Locate every Plasmodium parasite.
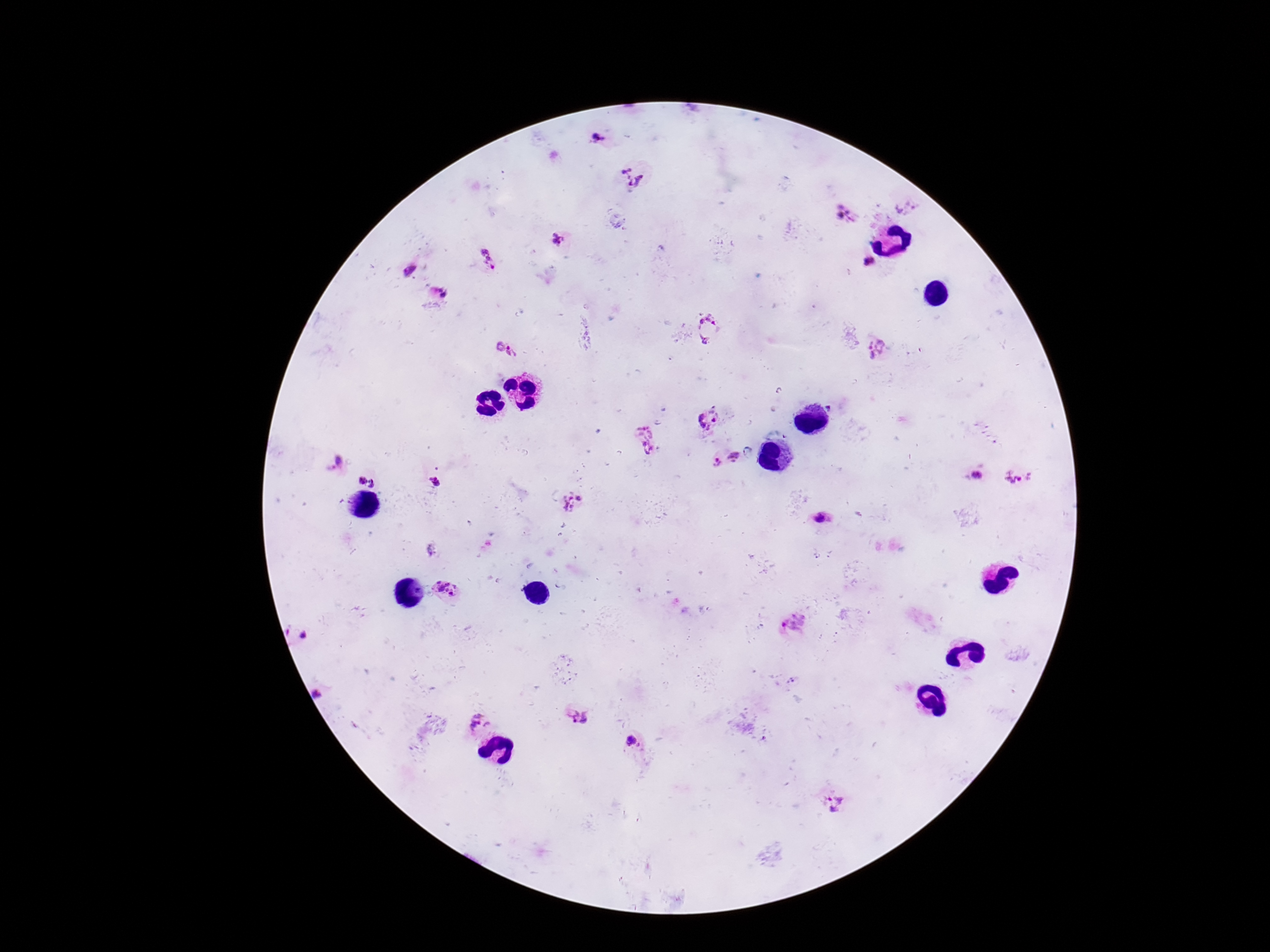

Approximate centers as [x, y] in pixels.
Plasmodium parasites: [599, 139], [632, 176], [906, 208], [846, 213], [558, 239], [487, 258], [868, 264], [409, 270], [442, 292], [708, 328], [499, 345], [877, 349], [512, 352], [831, 407], [708, 418], [646, 439], [736, 459], [337, 461], [714, 462], [980, 477], [1015, 478], [361, 480], [434, 482], [373, 483], [573, 504], [819, 519], [447, 587], [794, 624], [304, 636], [318, 694], [576, 716], [479, 723], [631, 742], [834, 803].

patient malaria status = infected
field of view = one from this slide
magnification = 100x
image size = 1270×952 pixels
preparation = thick blood film
stain = Giemsa
capture = smartphone camera through the microscope eyepiece